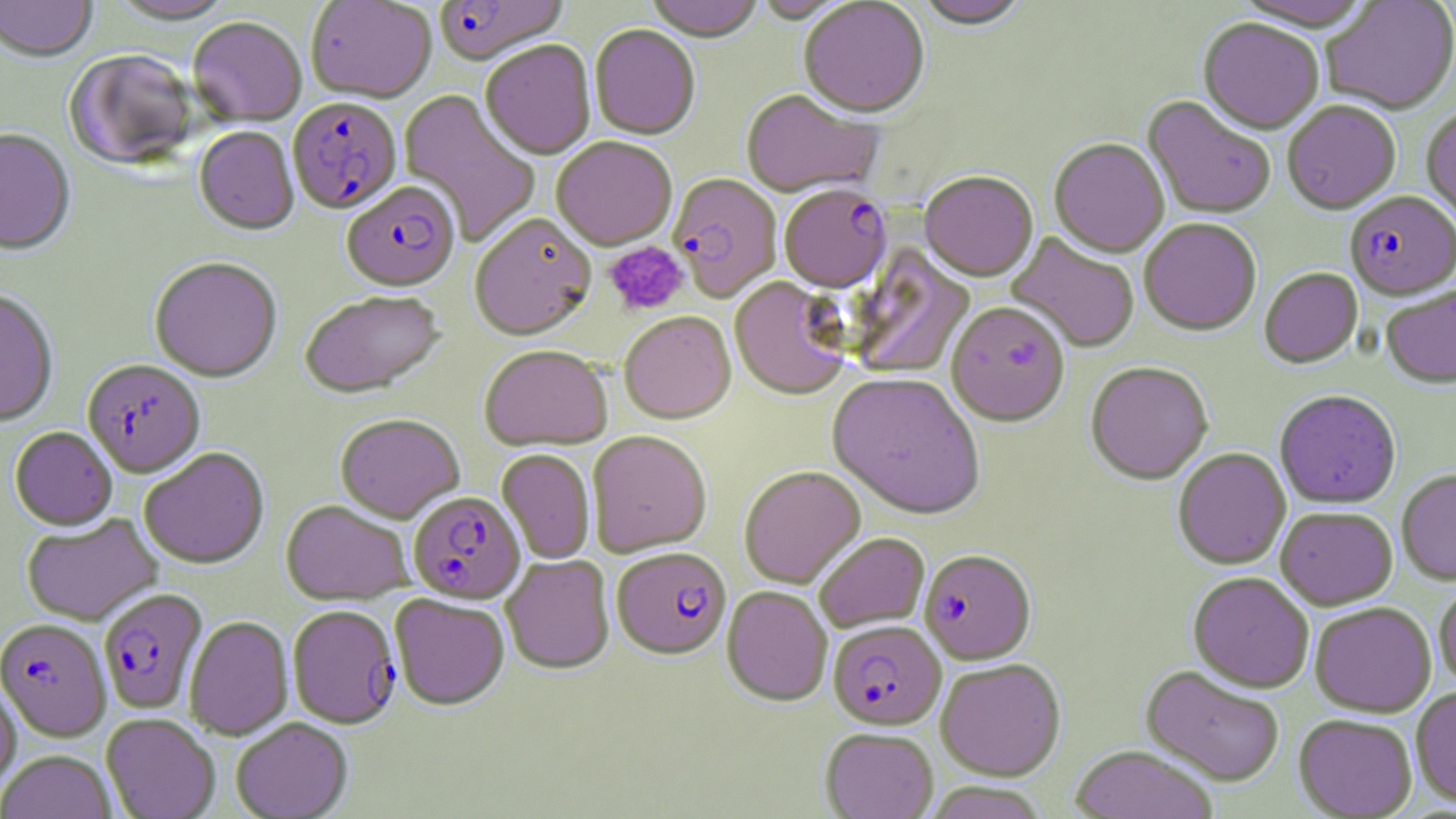

{
  "slide_level_diagnosis": "Plasmodium falciparum",
  "platelet_locations": "approximate bounding boxes as (x1, y1, x2, y2) in pixels: (603, 241, 689, 317)",
  "preparation": "thin blood smear",
  "stain": "May-Grünwald-Giemsa",
  "magnification": "1000x",
  "modality": "light microscopy",
  "uninfected_red_blood_cell_locations": "approximate bounding boxes as (x1, y1, x2, y2) in pixels: (0, 0, 98, 64), (106, 0, 239, 27), (305, 0, 437, 105), (646, 0, 764, 45), (753, 0, 858, 25), (1228, 0, 1377, 35), (1322, 0, 1456, 117), (798, 1, 930, 122), (914, 1, 1032, 33), (188, 19, 306, 128), (1197, 20, 1324, 137), (589, 26, 701, 142), (480, 43, 596, 162), (64, 52, 200, 173), (397, 90, 541, 247), (740, 91, 881, 200), (1141, 96, 1275, 220), (1282, 103, 1401, 216), (1421, 110, 1456, 231), (194, 127, 299, 237), (0, 130, 76, 257), (551, 139, 677, 252), (1048, 140, 1170, 260), (919, 174, 1038, 284), (469, 216, 597, 344), (1139, 220, 1261, 338), (1005, 233, 1140, 353), (846, 245, 976, 381), (149, 258, 283, 383), (1259, 269, 1363, 370), (729, 278, 851, 403), (1381, 286, 1456, 390), (0, 290, 59, 428), (300, 292, 446, 399), (946, 305, 1070, 430), (619, 312, 736, 426), (479, 346, 611, 452), (1085, 363, 1213, 488), (826, 375, 986, 523), (1274, 391, 1401, 510), (335, 414, 464, 524), (9, 427, 117, 531), (587, 432, 712, 558), (139, 447, 270, 569), (1172, 449, 1291, 571), (497, 450, 595, 565), (740, 468, 866, 590), (1397, 469, 1456, 586), (280, 500, 414, 605), (1275, 508, 1398, 611), (22, 514, 162, 626), (814, 534, 929, 634), (500, 555, 615, 675), (1187, 574, 1314, 694), (1434, 582, 1456, 691), (721, 587, 832, 707), (389, 594, 510, 711), (1309, 603, 1436, 718), (184, 615, 294, 741), (935, 660, 1067, 782), (1140, 666, 1285, 787), (0, 679, 21, 798), (1410, 688, 1456, 809), (101, 713, 220, 819), (1293, 715, 1417, 818), (231, 717, 353, 819), (820, 729, 938, 819), (1070, 746, 1217, 819), (0, 750, 117, 819), (923, 783, 1050, 819)",
  "field_of_view": "one of a larger specimen",
  "image_size": "1456×819 pixels",
  "plasmodium_falciparum_infected_red_blood_cell_locations": "approximate bounding boxes as (x1, y1, x2, y2) in pixels: (433, 0, 569, 69), (287, 99, 403, 216), (667, 175, 782, 303), (342, 183, 460, 295), (779, 187, 891, 295), (1344, 193, 1456, 303), (82, 360, 205, 478), (407, 491, 525, 605), (611, 549, 732, 662), (919, 551, 1036, 667), (99, 587, 208, 715), (287, 604, 401, 730), (0, 619, 112, 742), (827, 622, 946, 731)"
}